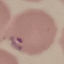
result = malaria parasites detected
image type = automatically extracted cell patch, resized to 64 × 64 pixels
capture = smartphone through the microscope eyepiece
preparation = thin smear
stain = Giemsa